Report the malaria status of this cell.
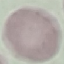

Uninfected.

Automatically extracted cell patch, resized to 64 × 64 pixels. Thin blood film. Photographed with a smartphone camera at the microscope eyepiece. Giemsa stain.